Locate every Plasmodium parasite.
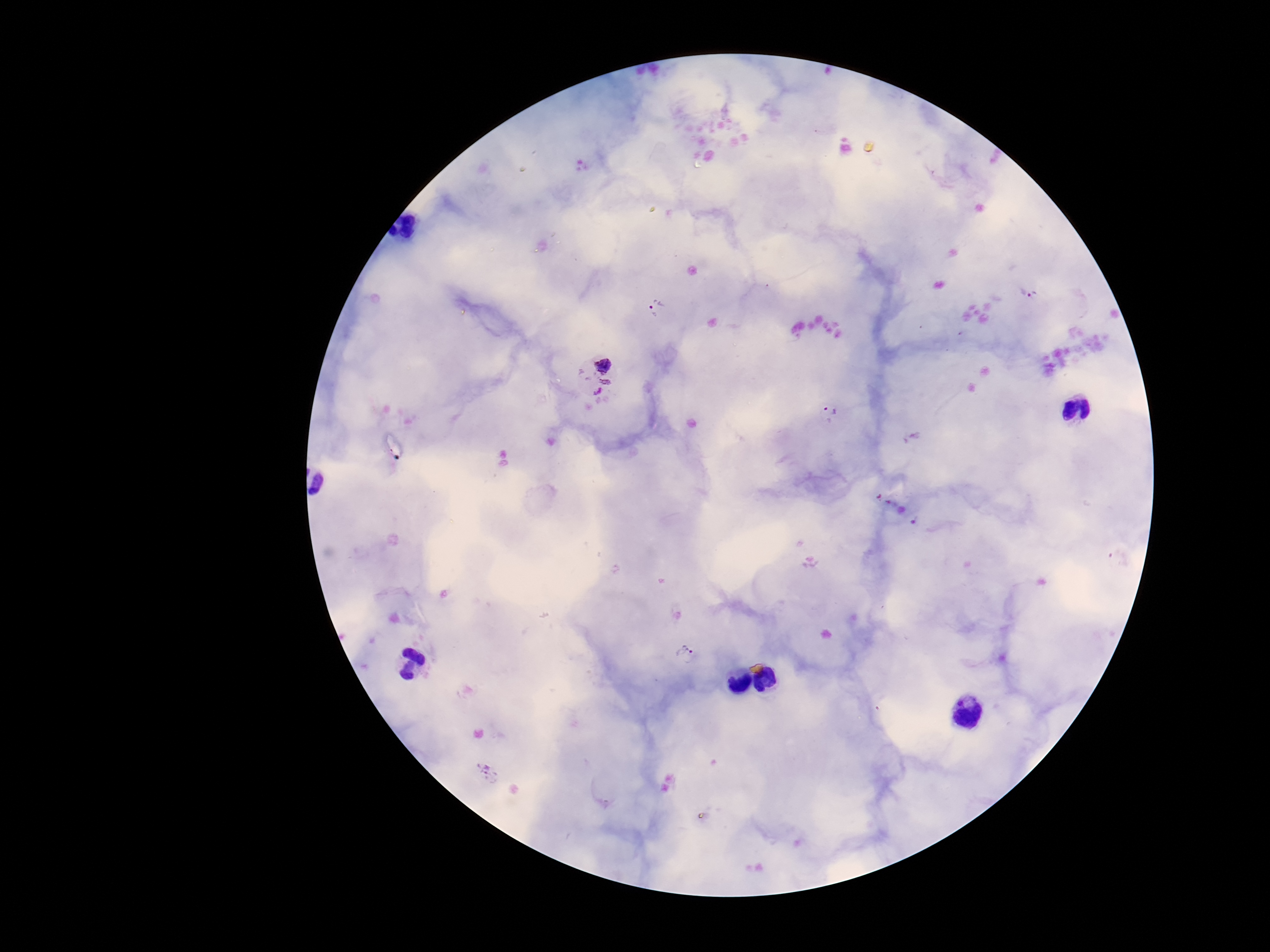
Approximate centers as [x, y] in pixels.
Plasmodium parasites: [1035, 297], [656, 308], [594, 374], [831, 408], [685, 654], [489, 773].

preparation = thick peripheral-blood smear
capture = smartphone camera through the microscope eyepiece
magnification = 100x
stain = Giemsa
image size = 1270×952 pixels
field of view = one from this slide
patient malaria status = infected